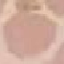
Result: no malaria parasites seen. Thin blood smear. Cell patch, automatically extracted from a larger field of view and resized to 64 × 64 pixels. Photographed with a smartphone camera at the microscope eyepiece. Giemsa-stained preparation.